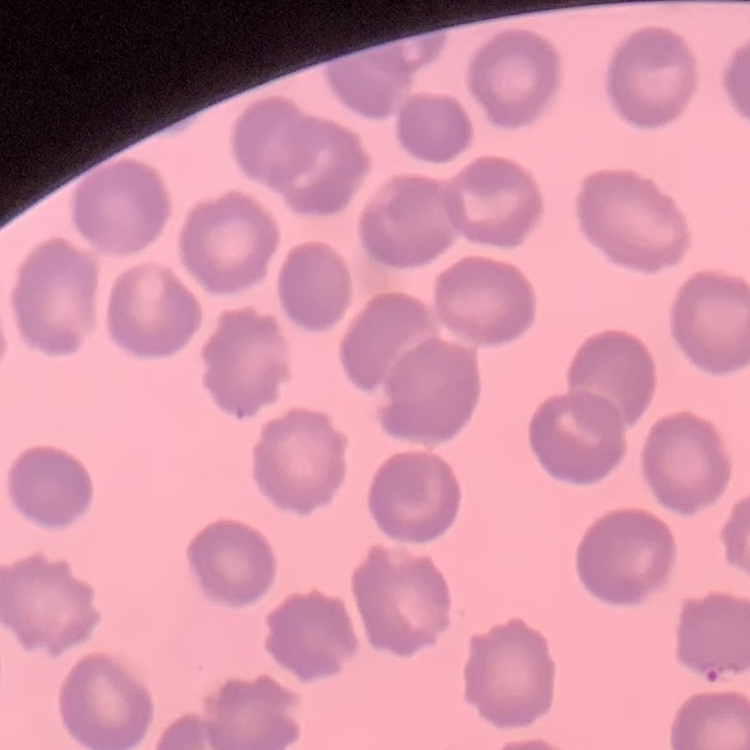
The red blood cells show no rouleaux formation. Thin peripheral smear. Stained with either Field's or Giemsa. Square crop of a larger photomicrograph.